Point out each leukocyte.
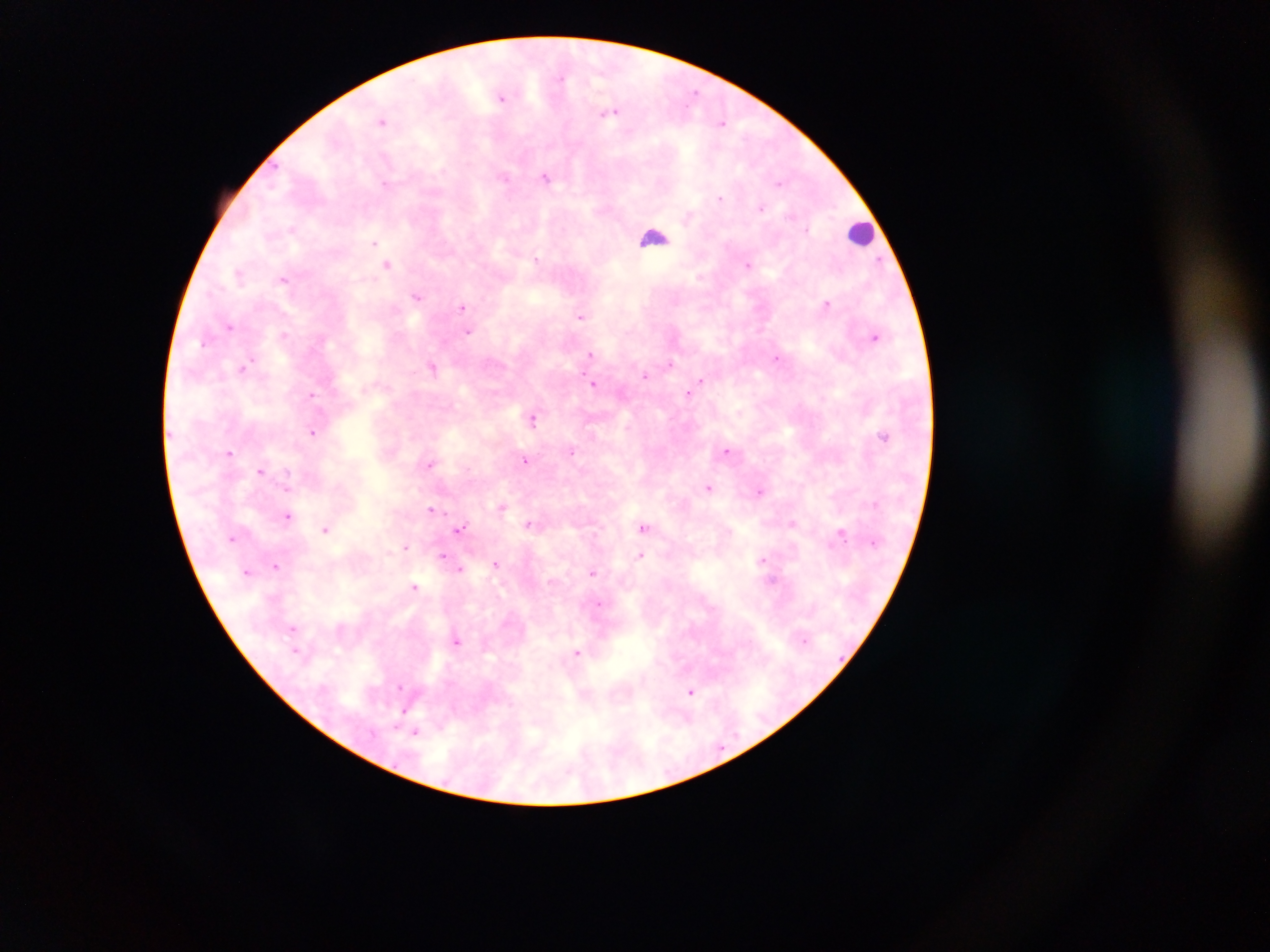

Approximate centers as (x, y) in pixels.
Leukocytes: (861, 233), (654, 237).

Plasmodium parasite locations: (561, 78), (696, 92), (501, 96), (611, 113), (382, 121), (723, 123), (504, 177), (546, 177), (384, 184), (780, 184), (721, 198), (761, 208), (292, 229), (807, 229), (374, 243), (536, 259), (880, 260), (388, 264), (747, 265), (238, 274), (284, 280), (417, 296), (826, 304), (462, 307), (580, 316), (230, 326), (468, 332), (284, 334), (875, 336), (205, 342), (590, 354), (776, 358), (251, 360), (670, 363), (247, 366), (432, 367), (645, 375), (701, 380), (594, 383), (688, 394), (311, 395), (532, 419), (313, 431), (884, 435), (727, 451), (230, 452), (572, 452), (525, 460), (430, 465), (260, 470), (288, 473), (708, 488), (760, 492), (501, 507), (431, 509), (287, 516), (529, 524), (792, 524), (643, 527), (326, 529), (460, 529), (840, 533), (233, 538), (405, 547), (443, 555), (641, 555), (762, 560), (495, 564), (276, 565), (460, 569), (592, 573), (415, 587), (598, 604), (293, 628), (457, 641), (296, 650), (577, 653), (399, 686), (691, 692), (402, 712), (416, 732). Single field of view. Thick blood smear. Image is 1270×952 pixels. Sample from Ghana. Mobile-phone photograph taken through the microscope.